Point out each Plasmodium parasite.
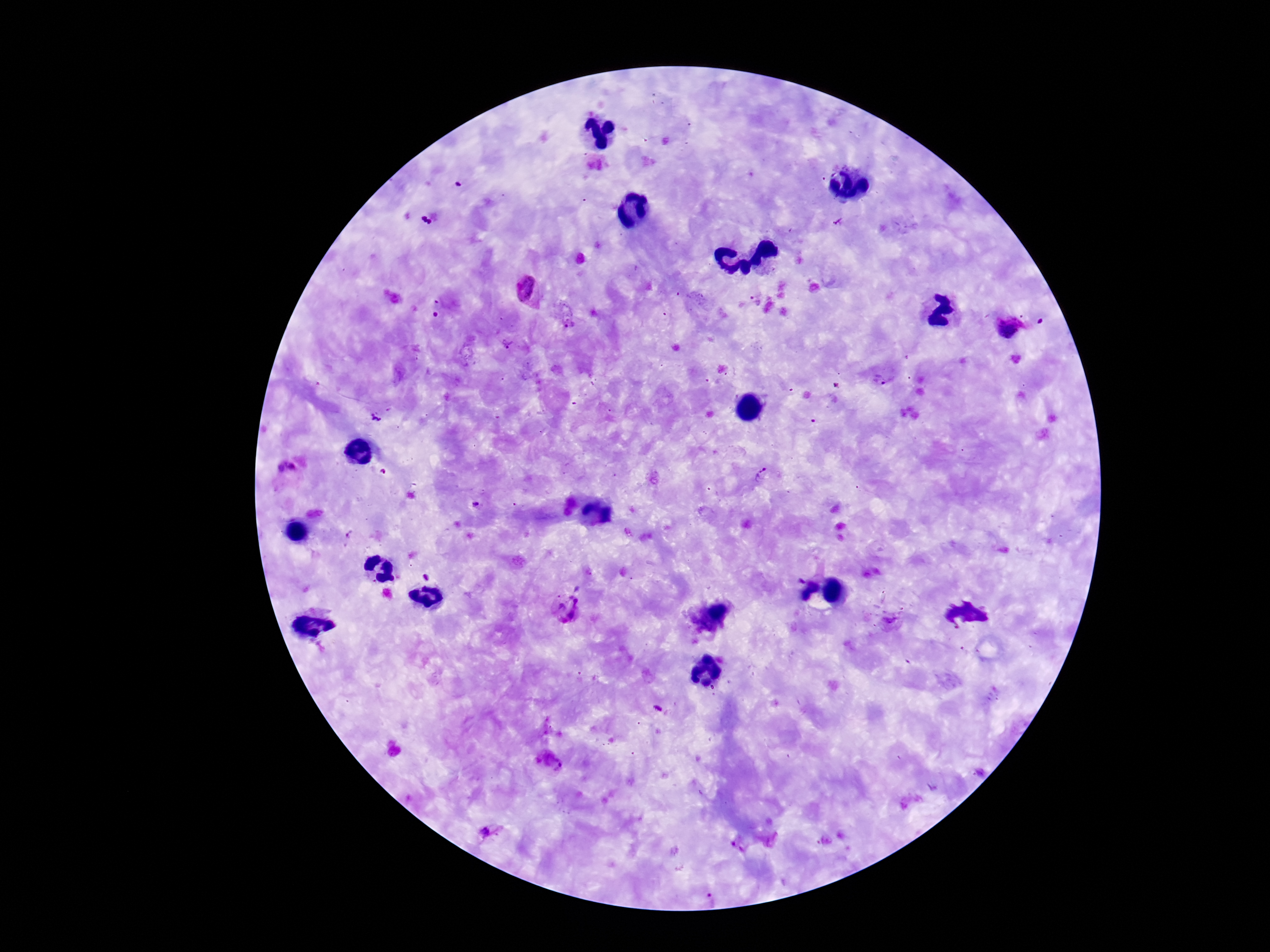
Approximate centers as {x, y} in pixels.
Plasmodium parasites: {430, 218}, {840, 223}, {526, 290}, {754, 299}, {572, 329}, {507, 344}, {880, 382}, {375, 417}, {285, 469}, {382, 472}, {763, 475}, {476, 505}, {351, 534}, {580, 586}, {569, 608}, {552, 763}, {488, 833}, {710, 900}.

magnification = 100x
image size = 1270×952 pixels
preparation = thick peripheral-blood smear
field of view = one from this slide
capture = smartphone camera through the microscope eyepiece
patient malaria status = positive
stain = Giemsa